Classify this cell by malaria status.
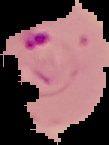
It is parasitized.

image size = 109×145 pixels
image type = cell region segmented out of the field of view; surrounding area masked to black
preparation = thin blood smear